Comment on the morphology of the red blood cells.
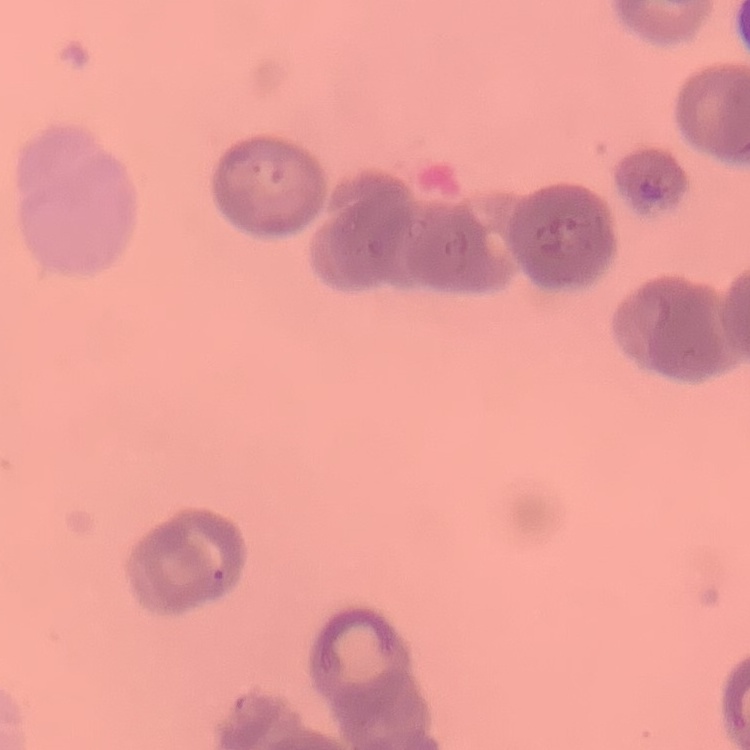
Rouleaux formation.

Summary:
  - Stain: Field's or Giemsa
  - Image type: square crop of a larger photomicrograph
  - Preparation: thin blood smear